Evaluate for Plasmodium parasites.
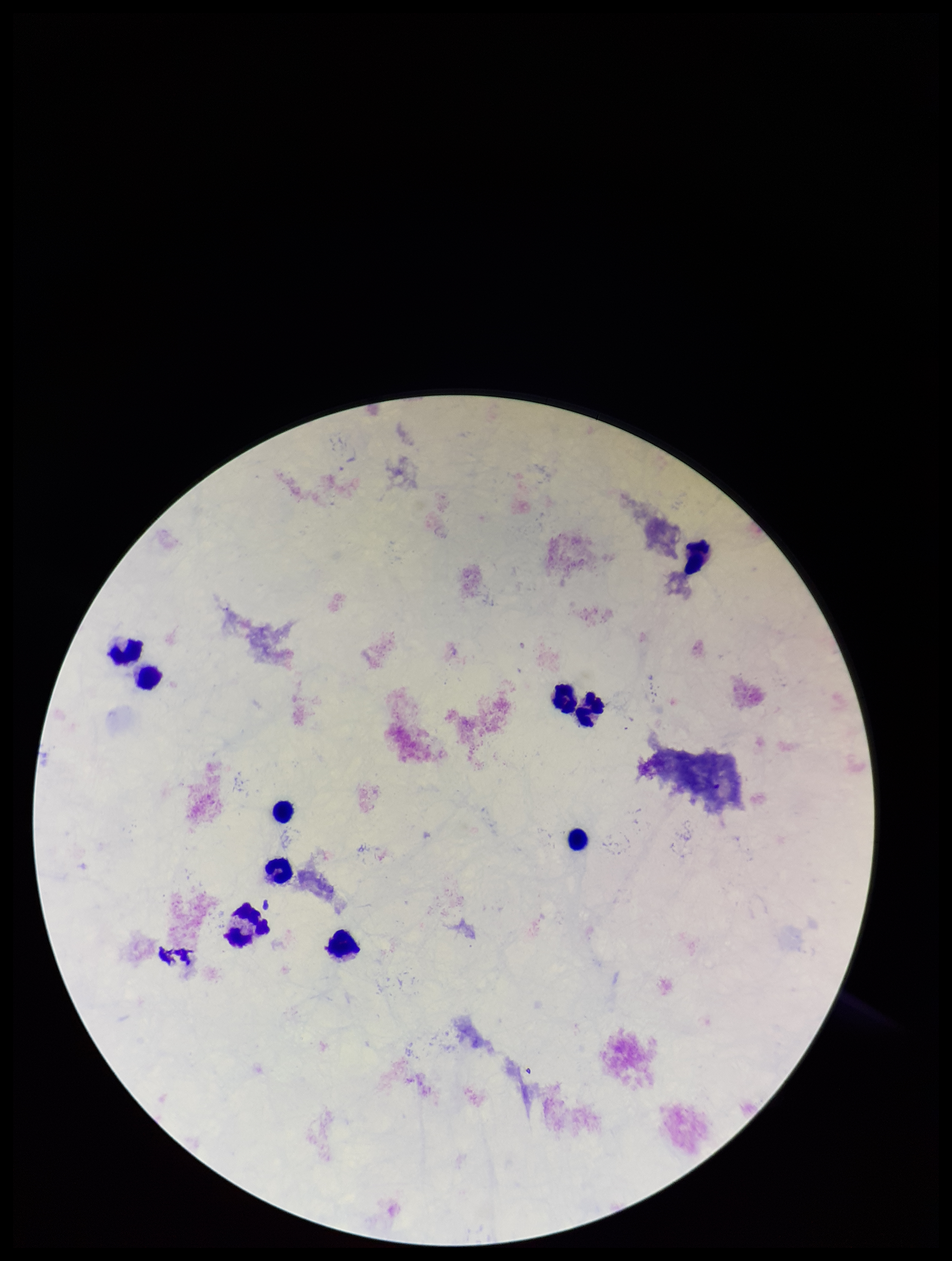
None seen.

Summary:
  - Leukocyte count: 10
  - Capture: smartphone photograph through the microscope eyepiece
  - Preparation: thick smear
  - Image size: 952×1261 pixels
  - Patient malaria status: negative
  - Parasite count: 0
  - Stain: Giemsa
  - Field of view: single